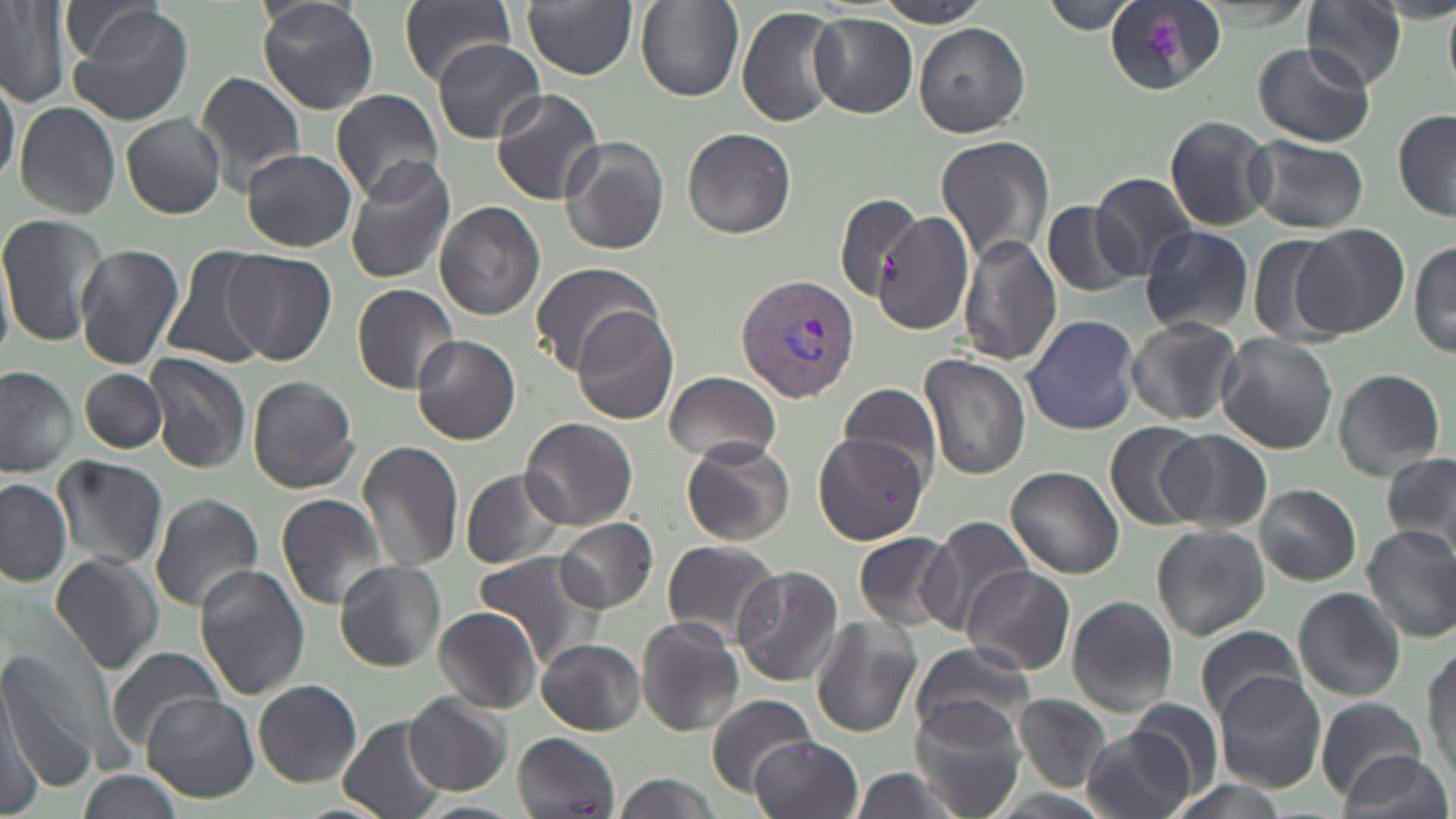

Approximate bounding boxes as (x1,y1)-(x2,y2) corner pairs in pixels. Plasmodium vivax-infected red blood cell locations: (736,273)-(860,404). Platelet locations: (1143,17)-(1185,65). Uninfected red blood cell locations: (60,0)-(174,72), (257,0)-(378,114), (399,0)-(517,86), (522,0)-(636,79), (1041,0)-(1135,35), (636,1)-(743,102), (873,1)-(992,27), (0,2)-(69,107), (1302,2)-(1406,90), (1105,3)-(1222,95), (64,4)-(198,127), (737,6)-(844,127), (808,14)-(917,116), (914,23)-(1031,137), (432,39)-(545,143), (1253,42)-(1374,149), (0,68)-(19,191), (196,72)-(307,188), (330,88)-(444,203), (491,89)-(606,205), (15,102)-(120,217), (1393,109)-(1455,223), (122,113)-(226,219), (1164,115)-(1275,231), (681,127)-(797,238), (560,135)-(670,255), (935,135)-(1054,267), (1244,136)-(1369,234), (243,149)-(358,252), (343,157)-(457,286), (1090,173)-(1199,276), (834,193)-(919,299), (1041,200)-(1142,297), (435,202)-(545,321), (877,211)-(974,334), (0,215)-(106,346), (1294,223)-(1408,338), (1140,226)-(1255,335), (1247,232)-(1345,344), (957,235)-(1061,367), (1411,235)-(1456,362), (74,243)-(184,370), (161,246)-(271,369), (225,249)-(337,365), (527,261)-(661,374), (352,282)-(460,393), (571,306)-(680,425), (1022,314)-(1141,435), (1126,318)-(1243,426), (410,334)-(521,445), (1217,334)-(1338,453), (146,353)-(251,474), (920,355)-(1031,480), (0,365)-(79,477), (80,368)-(166,453), (1333,368)-(1445,478), (664,370)-(782,465), (246,374)-(361,493), (837,381)-(941,483), (521,417)-(638,531), (1103,421)-(1209,531), (1161,430)-(1273,533), (816,434)-(927,544), (358,440)-(465,574), (681,441)-(797,546), (1381,451)-(1456,561), (55,455)-(168,570), (1006,466)-(1124,580), (460,469)-(570,570), (0,478)-(72,587), (1256,485)-(1362,585), (149,492)-(263,614), (275,493)-(388,609), (922,515)-(1037,630), (556,517)-(658,612), (1154,524)-(1269,640), (1361,525)-(1456,640), (853,529)-(962,635), (661,539)-(781,645), (474,550)-(605,670), (51,553)-(164,676), (1322,557)-(1445,691), (335,561)-(445,670), (961,564)-(1074,676), (194,565)-(310,700), (730,566)-(844,687), (1293,587)-(1407,701), (1066,595)-(1178,717), (433,606)-(544,713), (636,617)-(744,735), (810,617)-(920,738), (1194,623)-(1304,724), (1424,638)-(1456,787), (537,639)-(646,734), (911,641)-(1034,743), (0,648)-(104,792), (108,649)-(225,752), (1216,675)-(1325,790), (3,676)-(50,810), (254,680)-(362,786), (404,692)-(513,796), (142,693)-(258,803), (705,693)-(817,797), (1013,693)-(1113,791), (1316,697)-(1425,799), (1127,698)-(1222,795), (913,704)-(1029,819), (339,717)-(448,819), (1084,727)-(1195,819), (513,731)-(620,816), (751,736)-(863,819), (1337,750)-(1450,819), (844,768)-(965,819), (78,771)-(184,819), (611,773)-(724,819). Slide-level diagnosis: Plasmodium vivax. Captured at 1000x magnification. Image is 1456×819 pixels. May-Grünwald-Giemsa-stained preparation. Single field of view. Optical microscopy. Thin blood smear.